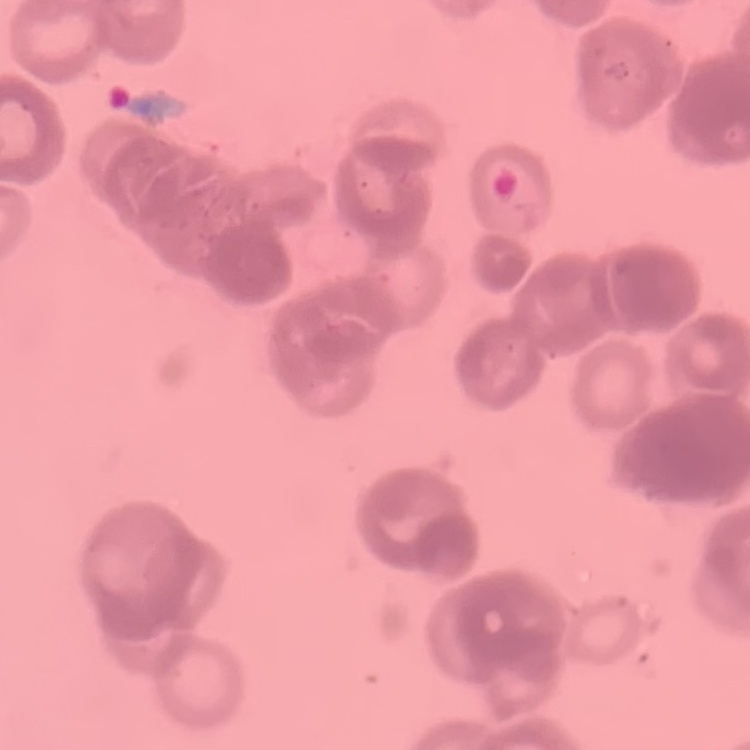

red blood cell morphology = rouleaux formation
stain = Field's or Giemsa
preparation = thin blood film
image type = one tile cut from a larger photomicrograph